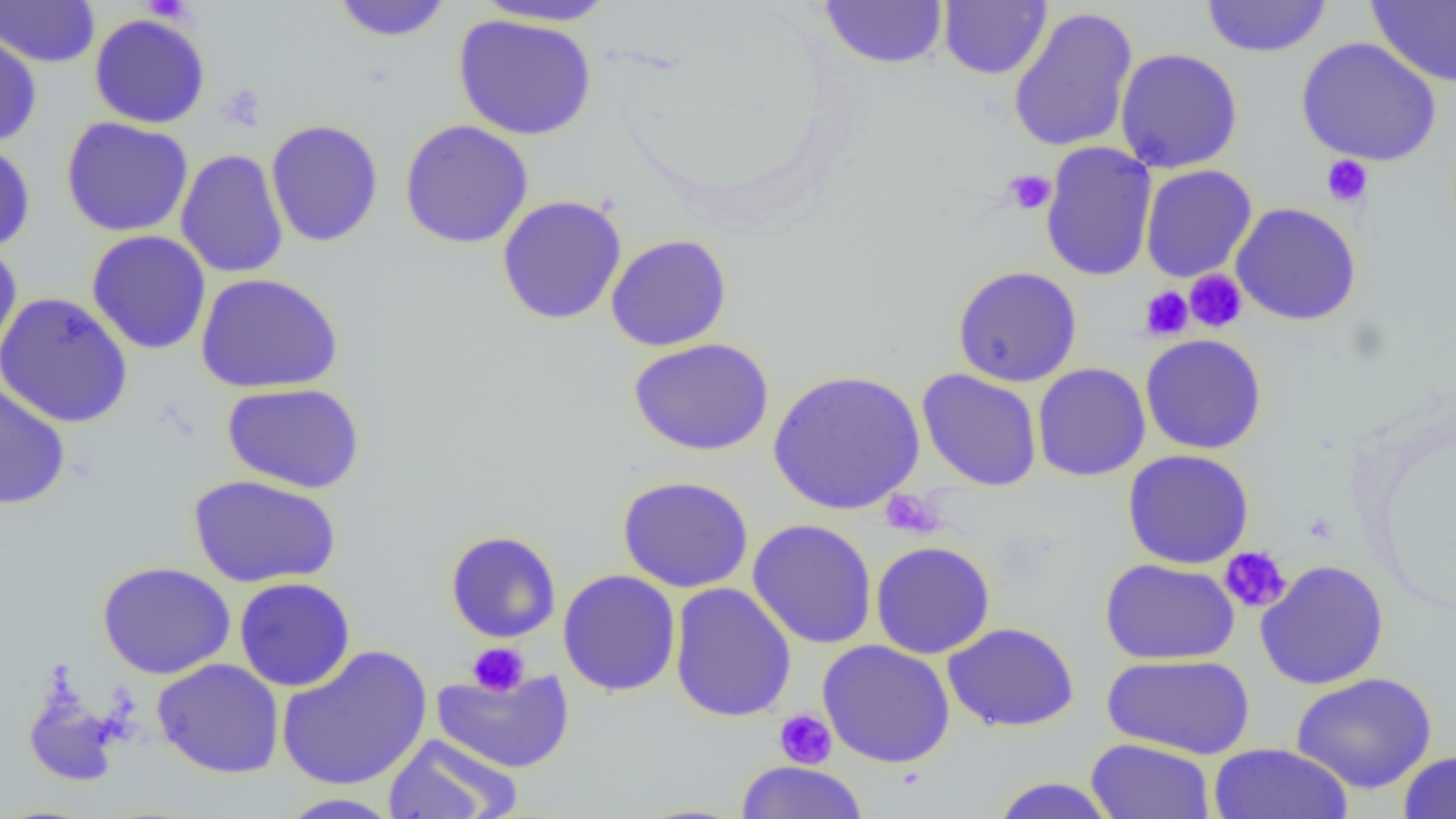
Summary:
  - Coordinate format: approximate bounding boxes as [x1, y1, x2, y2] in pixels
  - Uninfected red blood cell locations: [0, 0, 100, 68], [820, 0, 949, 70], [1200, 0, 1332, 58], [1366, 0, 1456, 88], [329, 1, 454, 43], [471, 1, 622, 28], [938, 1, 1052, 80], [1007, 6, 1138, 153], [88, 13, 211, 129], [453, 14, 597, 141], [0, 28, 42, 146], [1296, 37, 1442, 167], [1114, 48, 1243, 174], [60, 117, 193, 237], [399, 119, 534, 249], [265, 120, 384, 247], [0, 140, 36, 254], [1040, 141, 1157, 282], [175, 149, 289, 279], [1140, 164, 1257, 283], [496, 195, 627, 325], [1231, 202, 1361, 326], [86, 230, 212, 355], [605, 234, 732, 352], [0, 240, 23, 365], [951, 265, 1083, 388], [195, 273, 344, 394], [0, 291, 133, 429], [1139, 334, 1268, 454], [628, 338, 774, 457], [1032, 362, 1150, 482], [768, 369, 926, 515], [917, 369, 1042, 492], [0, 382, 71, 510], [222, 382, 365, 494], [1121, 449, 1255, 569], [187, 474, 342, 588], [617, 476, 754, 593], [747, 518, 878, 649], [446, 530, 562, 643], [870, 541, 995, 659], [1100, 558, 1239, 665], [1255, 559, 1389, 690], [97, 561, 235, 679], [557, 569, 681, 697], [233, 577, 356, 692], [668, 582, 797, 722], [943, 622, 1079, 733], [817, 640, 956, 768], [275, 644, 433, 791], [1102, 653, 1254, 759], [152, 658, 284, 778], [431, 668, 575, 774], [1291, 672, 1437, 794], [21, 680, 127, 789], [382, 733, 522, 818], [1085, 738, 1215, 819], [1207, 743, 1353, 818], [1397, 749, 1456, 818], [734, 760, 869, 819], [989, 776, 1120, 818], [275, 792, 404, 818]
  - Platelet locations: [217, 82, 268, 131], [1321, 155, 1373, 208], [1003, 168, 1056, 215], [1185, 270, 1247, 332], [1139, 286, 1193, 341], [879, 489, 944, 539], [1219, 546, 1291, 614], [467, 642, 530, 695], [774, 708, 837, 769]
  - Slide-level diagnosis: negative for blood parasites
  - Modality: optical microscopy
  - Field of view: one of a larger specimen
  - Preparation: thin blood smear
  - Magnification: 1000x
  - Image size: 1456×819 pixels